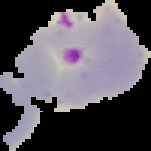

image type = segmented cell region on a black background
image size = 151×151 pixels
malaria status = parasitized
preparation = thin blood film